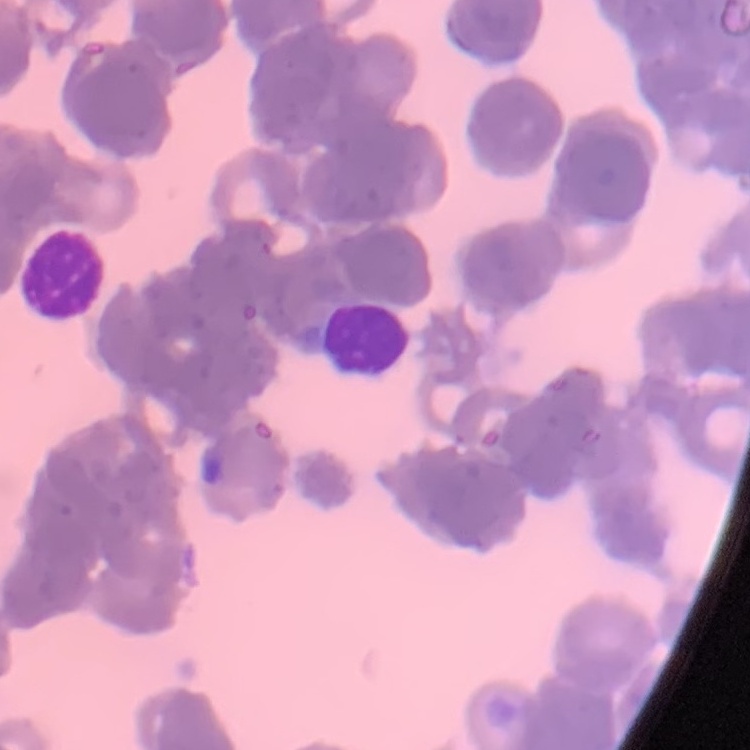

red blood cell morphology = rouleaux formation
stain = Field's or Giemsa
preparation = thin peripheral smear
image type = one tile cut from a larger photomicrograph